Point out cells.
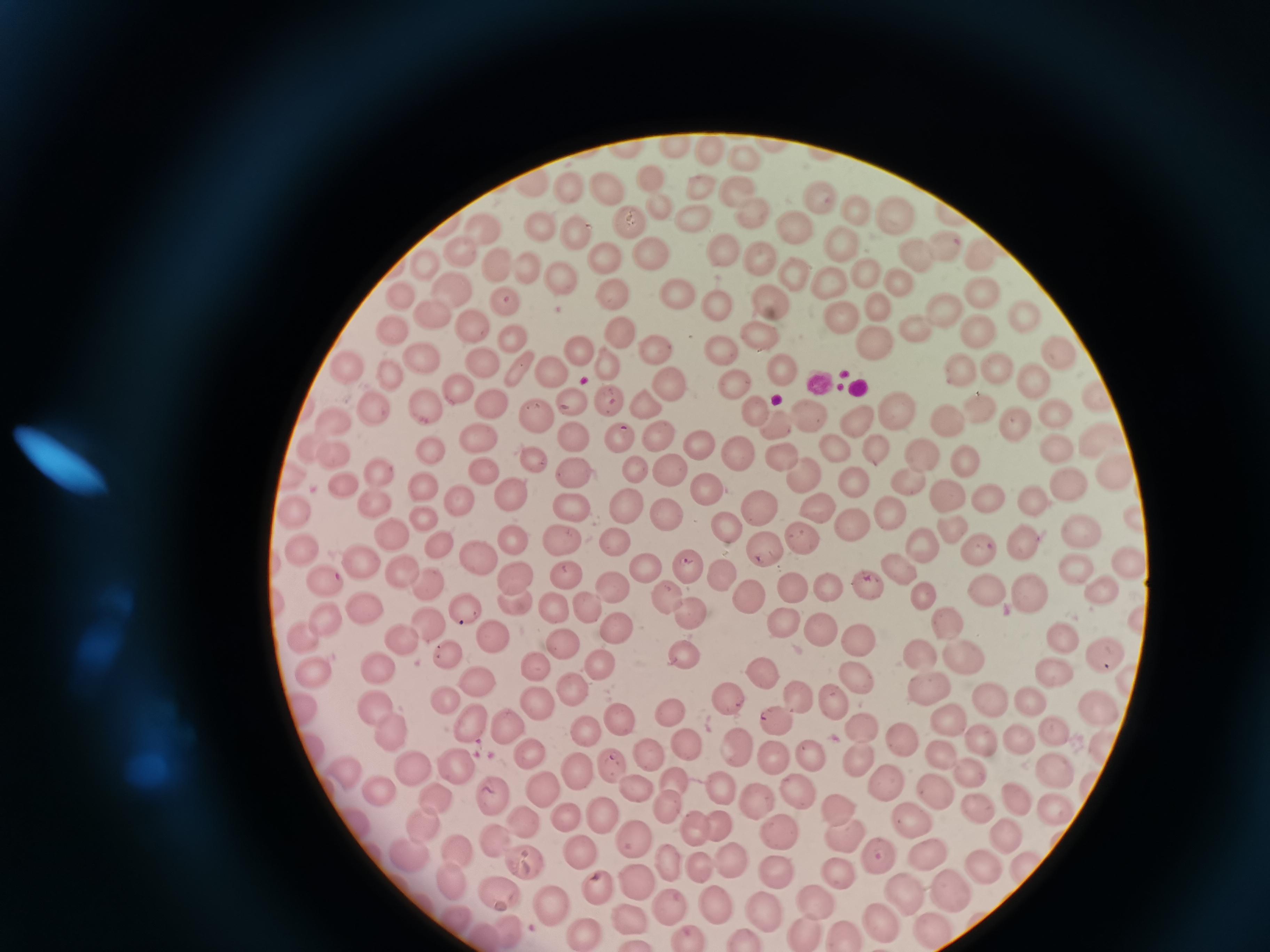
Approximate centers as [x, y] in pixels.
Cells: [773, 145], [674, 149], [705, 149], [743, 157], [649, 175], [530, 182], [564, 185], [603, 185], [734, 185], [699, 187], [822, 200], [858, 206], [660, 208], [894, 213], [690, 215], [750, 216], [625, 221], [800, 227], [482, 229], [542, 229], [579, 236], [840, 244], [461, 250], [942, 250], [645, 251], [726, 251], [919, 252], [605, 256], [761, 258], [987, 260], [505, 262], [424, 264], [534, 271], [796, 274], [565, 279], [869, 279], [901, 282], [832, 283], [455, 288], [679, 290], [404, 294], [765, 294], [982, 295], [614, 297], [506, 301], [720, 306], [944, 310], [430, 311], [843, 318], [1024, 322], [474, 328], [399, 330], [917, 330], [764, 331], [981, 332], [625, 334], [512, 337], [873, 340], [655, 345], [721, 350], [579, 351], [1055, 355], [425, 358], [485, 360], [995, 362], [352, 365], [785, 366], [608, 367], [959, 368], [392, 370], [522, 372], [553, 374], [1029, 379], [669, 380], [733, 381], [1096, 393], [462, 397], [427, 403], [610, 403], [650, 403], [493, 405], [571, 405], [979, 408], [755, 410], [898, 411], [1056, 412], [380, 413], [534, 416], [810, 417], [856, 417], [947, 417], [1016, 419], [333, 420], [778, 427], [571, 433], [1100, 435], [658, 438], [620, 439], [481, 442], [703, 444], [832, 445], [1056, 447], [871, 448], [314, 450], [431, 451], [919, 452], [739, 455], [337, 456], [531, 461], [785, 461], [968, 461], [636, 464], [576, 469], [671, 470], [291, 473], [479, 473], [382, 475], [1116, 475], [806, 479], [345, 483], [912, 483], [426, 485], [856, 485], [706, 486], [1065, 486], [990, 493], [950, 494], [512, 495], [461, 497], [1032, 503], [572, 504], [377, 505], [300, 506], [628, 506], [760, 506], [821, 507], [892, 512], [422, 517], [667, 519], [726, 525], [855, 525], [950, 527], [1078, 531], [393, 535], [1022, 538], [915, 542], [305, 543], [440, 543], [507, 543], [760, 544], [564, 545], [613, 546], [977, 551], [473, 555], [1133, 557], [363, 559], [683, 562], [641, 565], [1075, 566], [402, 567], [896, 567], [724, 574], [514, 575], [566, 575], [429, 580], [327, 582], [827, 582], [864, 582], [610, 587], [1098, 587], [794, 589], [990, 590], [1029, 590], [667, 594], [744, 594], [925, 595], [515, 602], [371, 604], [465, 605], [585, 607], [550, 608], [686, 613], [785, 619], [430, 620], [944, 622], [333, 628], [818, 630], [615, 631], [1061, 633], [498, 636], [856, 636], [304, 637], [407, 643], [559, 648], [1103, 648], [446, 652], [682, 655], [922, 656], [963, 658], [601, 663], [383, 666], [763, 670], [537, 671], [857, 673], [1056, 673], [316, 675], [478, 680], [930, 687], [576, 691], [800, 695], [446, 698], [725, 698], [835, 699], [541, 700], [982, 700], [1032, 700], [304, 704], [376, 704], [1095, 708], [668, 710], [775, 716], [946, 716], [619, 720], [478, 728], [387, 729], [865, 729], [1050, 729], [513, 731], [589, 733], [899, 736], [1018, 737], [682, 741], [977, 742], [1101, 744], [773, 749], [738, 750], [810, 752], [941, 753], [533, 756], [651, 756], [860, 756], [1052, 763], [455, 765], [412, 766], [615, 766], [968, 767], [347, 771], [576, 772], [675, 779], [886, 779], [930, 782], [636, 787], [544, 788], [380, 790], [722, 790], [495, 792], [796, 795], [1021, 795], [437, 797], [761, 799], [1055, 804], [977, 807], [838, 808], [559, 810], [669, 810], [603, 815], [519, 818], [909, 819], [722, 823], [425, 825], [696, 828], [784, 832], [1008, 834], [494, 837], [841, 837], [634, 839], [410, 851], [459, 851], [878, 854], [930, 856], [582, 857], [732, 859], [526, 861], [980, 861], [670, 864], [702, 866], [775, 871], [838, 872], [638, 877], [449, 878], [595, 888], [955, 889], [901, 890], [501, 891], [817, 899], [716, 900], [548, 903], [671, 904], [764, 905], [632, 918], [881, 919], [934, 928], [506, 930], [584, 931], [802, 931], [847, 933], [743, 935], [690, 936].

One field from this slide. Image is 1270×952 pixels. Giemsa stain. Acquired by smartphone through the microscope eyepiece. Thin blood film.